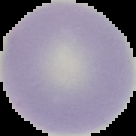

Summary:
  - Image type: segmented cell region with the area outside set to black
  - Preparation: thin blood film
  - Image size: 136×136 pixels
  - Result: negative for Plasmodium parasites